Identify the blood parasite species.
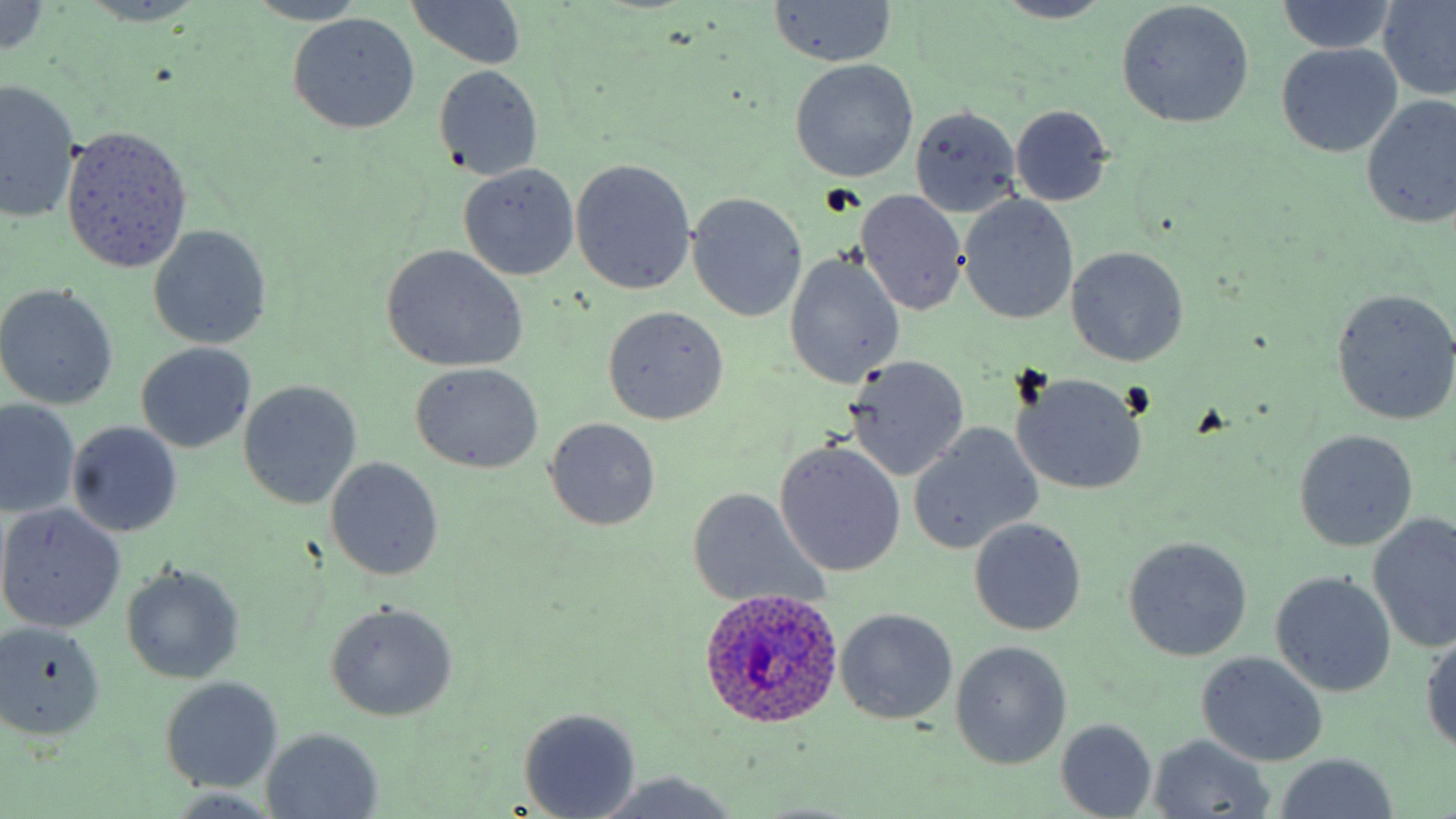
Plasmodium ovale.

{
  "modality": "light microscopy",
  "preparation": "thin blood smear",
  "field_of_view": "one of a larger specimen",
  "plasmodium_ovale_infected_red_blood_cell_locations": "approximate bounding boxes as named x1/y1/x2/y2 corners in pixels: (x1=697, y1=589, x2=845, y2=730)",
  "magnification": "1000x",
  "uninfected_red_blood_cell_locations": "approximate bounding boxes as named x1/y1/x2/y2 corners in pixels: (x1=1378, y1=0, x2=1456, y2=101), (x1=242, y1=1, x2=373, y2=27), (x1=405, y1=1, x2=528, y2=70), (x1=768, y1=1, x2=897, y2=67), (x1=990, y1=1, x2=1117, y2=24), (x1=1115, y1=1, x2=1254, y2=129), (x1=1276, y1=1, x2=1399, y2=54), (x1=0, y1=2, x2=54, y2=58), (x1=78, y1=2, x2=211, y2=27), (x1=288, y1=13, x2=421, y2=134), (x1=1275, y1=43, x2=1403, y2=158), (x1=791, y1=59, x2=919, y2=182), (x1=434, y1=65, x2=545, y2=181), (x1=0, y1=79, x2=82, y2=224), (x1=1360, y1=95, x2=1456, y2=231), (x1=909, y1=105, x2=1023, y2=216), (x1=1011, y1=106, x2=1112, y2=206), (x1=62, y1=125, x2=191, y2=272), (x1=570, y1=158, x2=696, y2=294), (x1=457, y1=163, x2=580, y2=281), (x1=856, y1=191, x2=968, y2=316), (x1=688, y1=192, x2=808, y2=322), (x1=958, y1=195, x2=1079, y2=324), (x1=148, y1=226, x2=271, y2=349), (x1=380, y1=246, x2=528, y2=373), (x1=1067, y1=247, x2=1189, y2=366), (x1=785, y1=254, x2=903, y2=387), (x1=0, y1=283, x2=119, y2=410), (x1=1329, y1=288, x2=1456, y2=425), (x1=601, y1=306, x2=729, y2=425), (x1=135, y1=342, x2=257, y2=453), (x1=844, y1=358, x2=971, y2=481), (x1=411, y1=362, x2=544, y2=473), (x1=1011, y1=373, x2=1148, y2=496), (x1=237, y1=381, x2=362, y2=509), (x1=1, y1=401, x2=78, y2=516), (x1=544, y1=417, x2=661, y2=530), (x1=66, y1=420, x2=184, y2=537), (x1=908, y1=425, x2=1042, y2=554), (x1=1292, y1=429, x2=1420, y2=551), (x1=775, y1=441, x2=906, y2=577), (x1=326, y1=456, x2=444, y2=580), (x1=685, y1=488, x2=825, y2=608), (x1=0, y1=503, x2=126, y2=632), (x1=1368, y1=513, x2=1456, y2=654), (x1=969, y1=518, x2=1087, y2=636), (x1=1123, y1=536, x2=1253, y2=661), (x1=121, y1=562, x2=244, y2=684), (x1=1270, y1=570, x2=1397, y2=697), (x1=325, y1=601, x2=457, y2=720), (x1=836, y1=608, x2=958, y2=726), (x1=0, y1=622, x2=105, y2=741), (x1=1420, y1=630, x2=1456, y2=756), (x1=950, y1=640, x2=1072, y2=770), (x1=1196, y1=651, x2=1329, y2=766), (x1=159, y1=676, x2=283, y2=793), (x1=518, y1=708, x2=640, y2=819), (x1=1056, y1=719, x2=1157, y2=817), (x1=261, y1=728, x2=383, y2=817), (x1=1147, y1=734, x2=1276, y2=816), (x1=1273, y1=754, x2=1397, y2=819), (x1=591, y1=773, x2=741, y2=819)",
  "image_size": "1456×819 pixels",
  "stain": "May-Grünwald-Giemsa"
}